Report the malaria status of this cell.
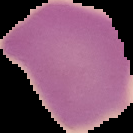
It is uninfected.

The area outside the segmented cell region is set to black. From a thin blood film. Image is 133×133 pixels.